Locate every leukocyte (white blood cell).
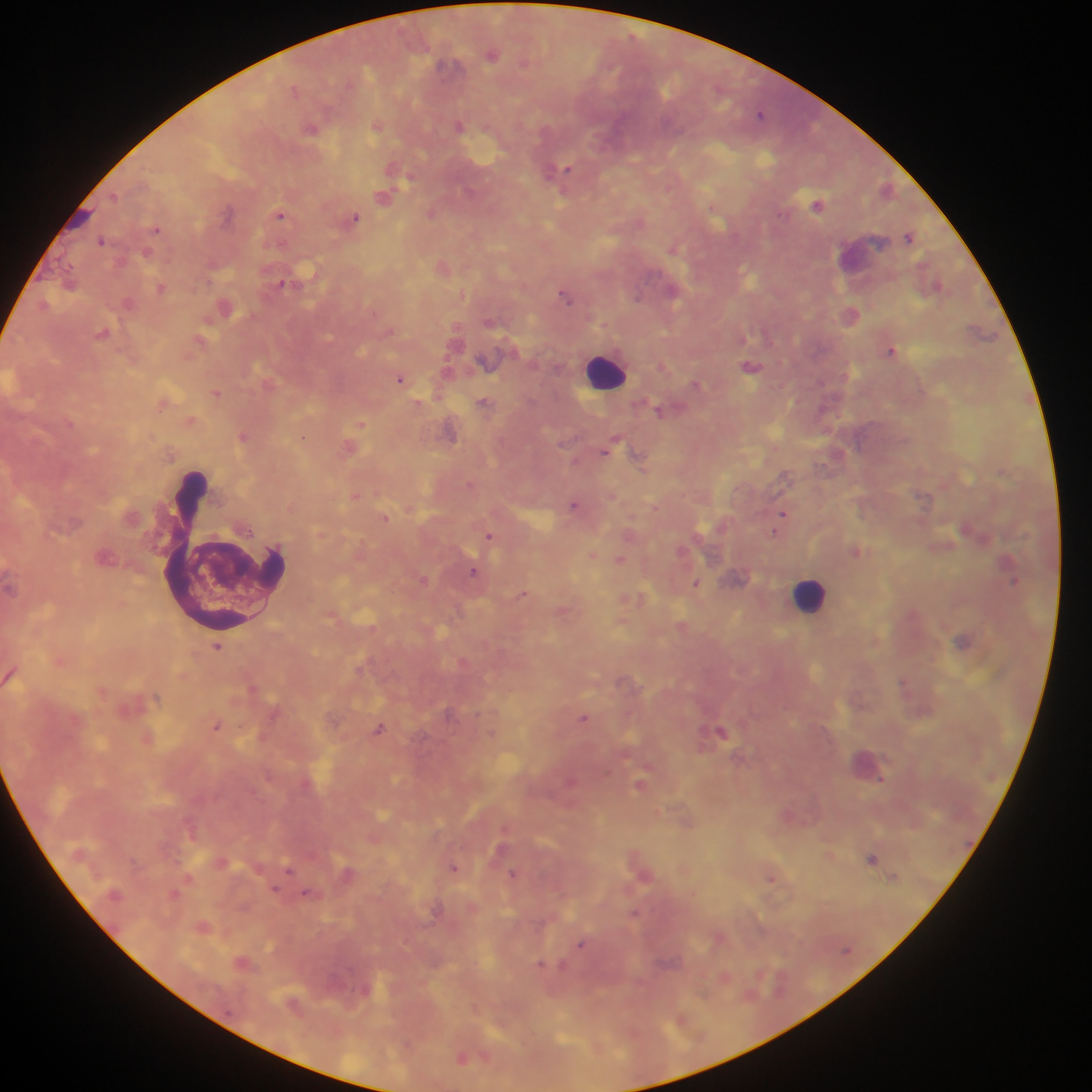

Approximate centers as (x, y) in pixels.
Leukocytes: (606, 372), (810, 596).

preparation: thick blood film
field_of_view: single
capture: mobile-phone photograph through a microscope
image_size: 1092×1092 pixels
country: Ghana
plasmodium_parasite_locations: 'approximate centers as (x, y) in pixels: (491, 54), (295, 89), (761, 114), (377, 125), (459, 125), (312, 129), (399, 169), (562, 170), (384, 196), (818, 204), (432, 212), (281, 214), (354, 218), (157, 228), (910, 235), (102, 240), (674, 247), (444, 268), (284, 282), (938, 286), (160, 287), (566, 295), (128, 303), (225, 306), (851, 313), (104, 332), (201, 341), (892, 349), (486, 362), (664, 366), (751, 366), (401, 377), (696, 383), (216, 393), (164, 402), (418, 403), (485, 404), (660, 410), (191, 420), (360, 423), (450, 430), (244, 436), (303, 437), (349, 447), (610, 447), (838, 453), (640, 458), (356, 495), (575, 504), (783, 514), (385, 517), (490, 535), (857, 551), (593, 554), (620, 559), (475, 571), (738, 577), (423, 579), (1014, 580), (696, 583), (523, 593), (636, 599), (564, 611), (622, 622), (682, 626), (964, 640), (218, 646), (60, 661), (905, 682), (254, 688), (584, 717), (217, 725), (380, 728), (721, 732), (148, 738), (867, 764), (882, 780), (571, 781), (641, 784), (788, 815), (830, 854), (873, 858), (455, 868), (290, 869), (642, 871), (348, 873), (514, 873), (190, 878), (772, 878), (276, 889), (175, 893), (309, 894), (636, 913), (203, 926), (720, 936), (582, 944), (243, 963), (543, 965), (562, 966), (725, 976), (682, 1019), (408, 1044), (463, 1058)'